Classify this cell by malaria status.
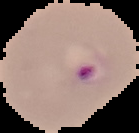
Parasitized.

preparation = thin blood smear
image type = segmented cell region on a black background
image size = 139×133 pixels